Identify the preparation type.
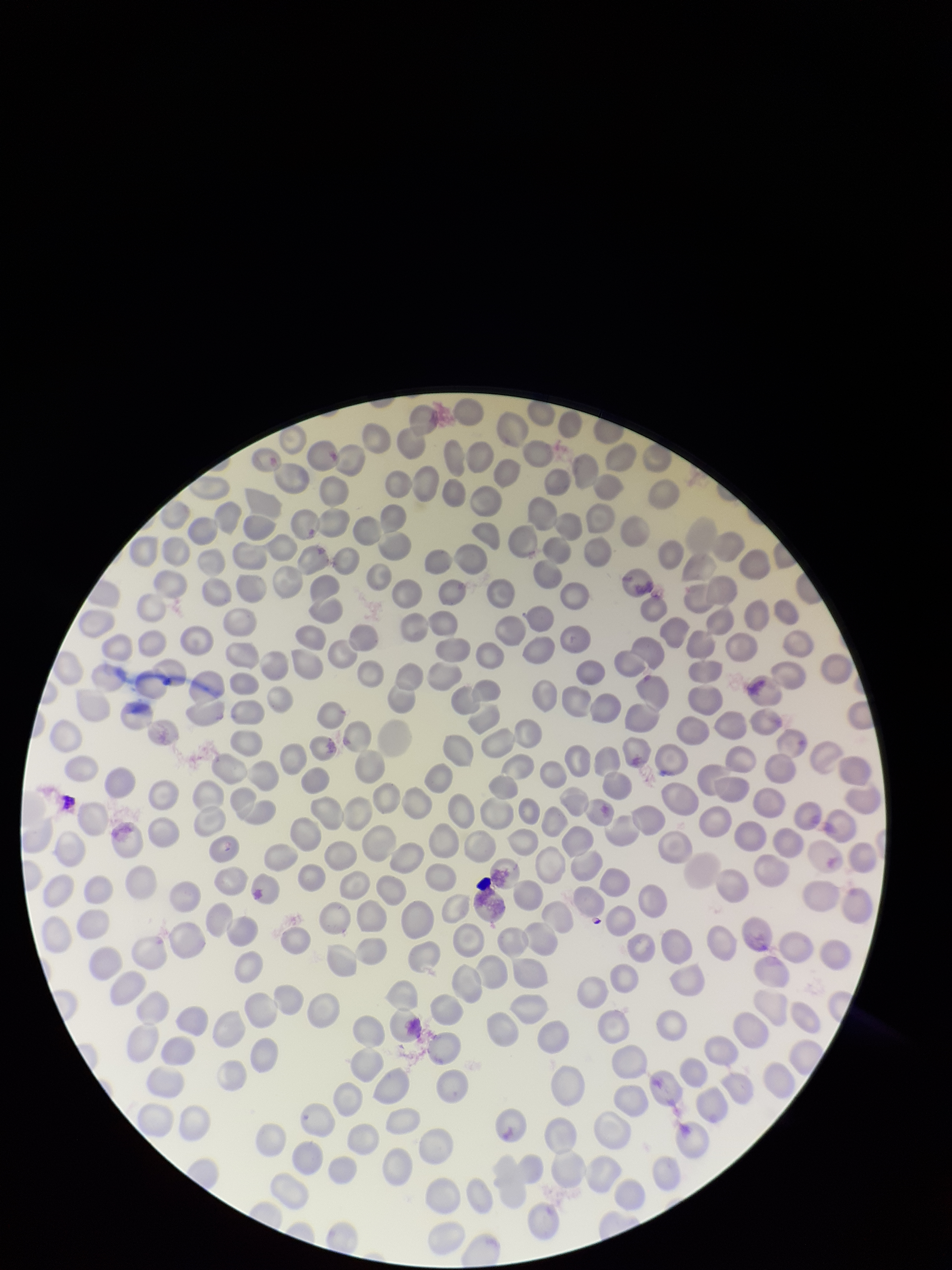

It is a thin blood smear.

Summary:
  - Parasitized red blood cells: none seen
  - Stain: Giemsa
  - Patient malaria status: negative
  - Capture: smartphone photograph through the microscope eyepiece
  - Parasitized red blood cell count: 0
  - Red blood cell count: 292
  - Field of view: one from this slide
  - Image size: 952×1270 pixels